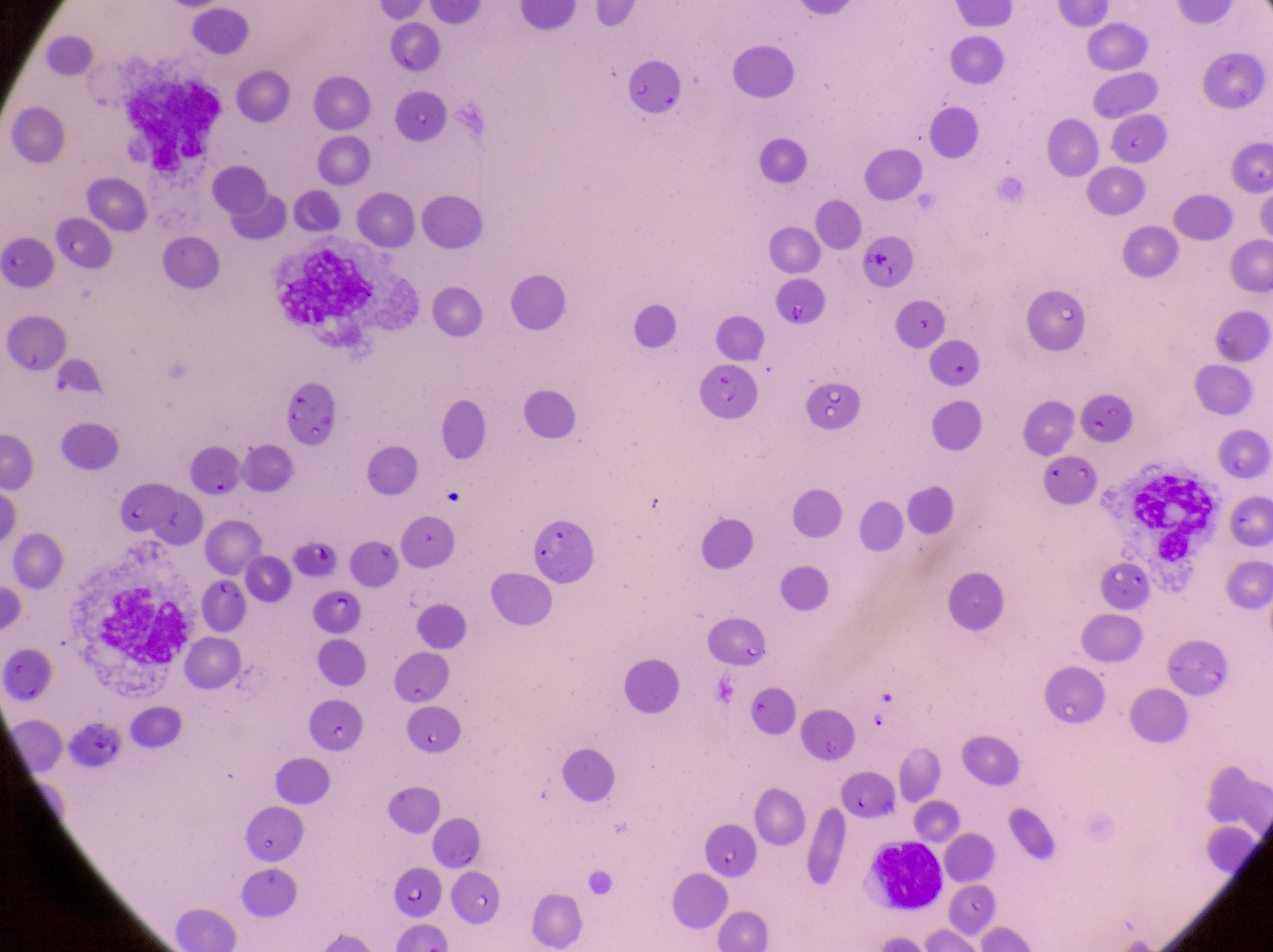

{
  "capture": "smartphone photograph through the eyepiece of an Olympus CX-23 microscope",
  "country": "Uganda",
  "preparation": "thin blood film",
  "magnification": "1000x",
  "field_of_view": "single",
  "leukocyte_locations": "approximate bounding boxes as {left, top, right, bottom} in pixels: {127, 85, 225, 182}, {99, 585, 188, 663}",
  "parasitised_red_blood_cell_locations": "approximate bounding boxes as {left, top, right, bottom} in pixels: {696, 367, 756, 419}, {205, 574, 252, 631}, {392, 856, 447, 914}",
  "image_size": "1273×952 pixels",
  "artifact_platelet_like_body_stain_precipitate_or_debris_locations": "approximate bounding boxes as {left, top, right, bottom} in pixels: {272, 247, 384, 330}, {100, 467, 177, 532}, {1138, 472, 1216, 569}"
}